Identify the parasite.
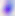
This is Toxoplasma gondii.

{
  "modality": "photomicrograph",
  "magnification": "400x"
}